Report the malaria status of this cell.
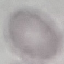
Uninfected.

Automatically extracted cell patch, resized to 64 × 64 pixels. Photographed with a smartphone camera at the microscope eyepiece. Giemsa-stained preparation. Thin blood smear.